Assess this cell for malaria.
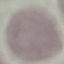
Uninfected.

Summary:
  - Capture: smartphone through the microscope eyepiece
  - Image type: automatically extracted cell patch, resized to 64 × 64 pixels
  - Stain: Giemsa
  - Preparation: thin blood film